Name the parasite shown.
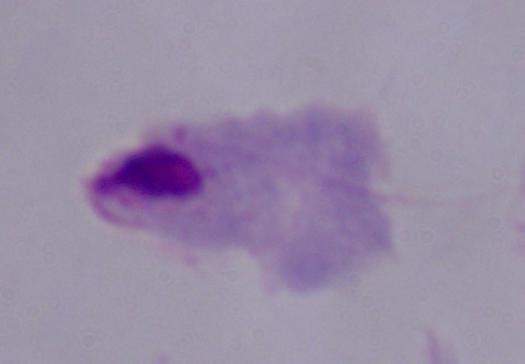

This is a trichomonad.

modality = photomicrograph
magnification = 1000x